Outline every parasitised red blood cell, every trophozoite, every gametocyte, every leukocyte, and every artifact (platelet-like body, stain precipitate, or debris).
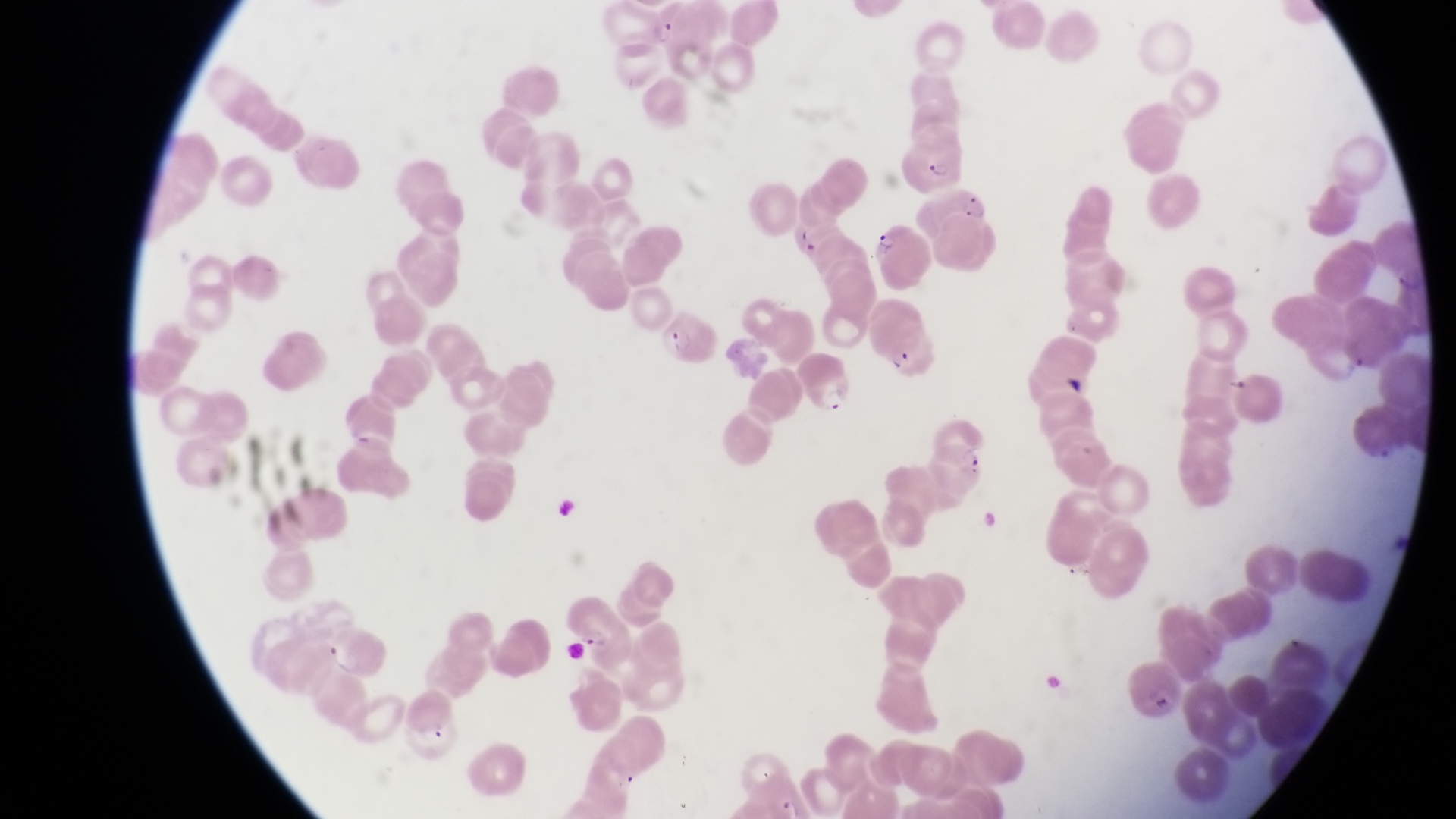

Approximate bounding boxes as (left, top, right, bottom) in pixels.
Parasitised red blood cells: (644, 7, 681, 50), (901, 136, 968, 191), (869, 224, 935, 288), (658, 300, 716, 367), (880, 315, 939, 387), (798, 354, 857, 420), (563, 598, 630, 659), (406, 691, 464, 761).
Trophozoites: (963, 193, 993, 225), (961, 442, 988, 474).
No leukocytes observed.

{
  "image_size": "1456×819 pixels",
  "preparation": "thin blood film",
  "field_of_view": "single",
  "magnification": "1000x",
  "country": "Uganda",
  "capture": "smartphone photograph through the eyepiece of an Olympus CX-23 microscope"
}